Assess this cell for malaria.
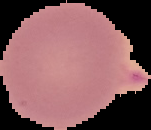
It is uninfected.

Image is 151×130 pixels. Segmented cell region on a black background. From a thin blood smear.